State which parasite is depicted.
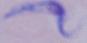
A trypanosome.

Summary:
  - Modality: micrograph
  - Magnification: 1000x